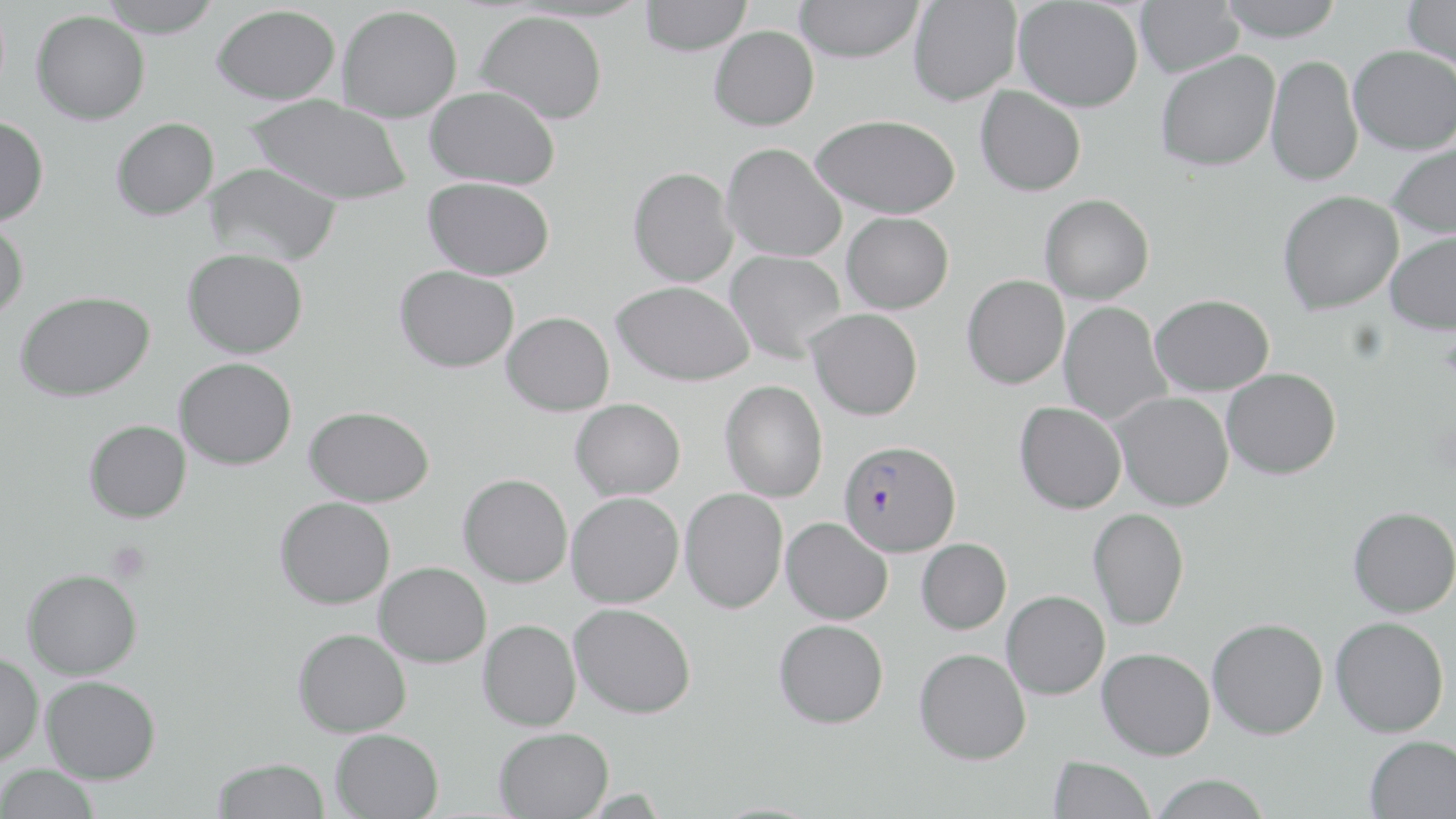
Approximate bounding boxes as [x1, y1, x2, y2] in pixels. Uninfected red blood cell locations: [97, 0, 223, 37], [640, 0, 751, 55], [1215, 0, 1344, 41], [1403, 0, 1456, 72], [794, 1, 924, 63], [908, 1, 1021, 106], [1014, 1, 1143, 112], [1135, 1, 1242, 77], [212, 4, 340, 105], [337, 5, 462, 123], [31, 10, 150, 125], [475, 10, 607, 124], [709, 25, 819, 130], [1348, 45, 1456, 155], [1155, 51, 1279, 172], [1265, 54, 1363, 187], [425, 85, 560, 189], [975, 86, 1086, 196], [247, 95, 412, 206], [810, 114, 961, 219], [0, 116, 49, 226], [111, 117, 219, 220], [1386, 140, 1456, 238], [722, 142, 847, 262], [203, 162, 342, 265], [628, 167, 738, 287], [422, 177, 554, 280], [1277, 190, 1403, 314], [1040, 194, 1154, 304], [842, 211, 954, 314], [0, 218, 29, 318], [1384, 232, 1456, 335], [182, 248, 308, 359], [725, 250, 846, 362], [394, 265, 519, 373], [961, 275, 1069, 389], [612, 280, 755, 386], [15, 291, 155, 402], [1149, 294, 1274, 396], [1058, 301, 1171, 425], [807, 309, 922, 420], [502, 311, 614, 415], [173, 357, 297, 470], [1221, 367, 1341, 479], [720, 380, 828, 501], [1110, 392, 1234, 511], [570, 398, 685, 500], [1014, 402, 1126, 514], [304, 406, 436, 506], [84, 419, 191, 523], [458, 473, 573, 587], [679, 487, 789, 613], [566, 492, 684, 607], [275, 497, 395, 609], [1347, 506, 1456, 618], [1088, 508, 1189, 630], [781, 517, 893, 624], [916, 539, 1011, 634], [374, 561, 491, 667], [22, 568, 142, 679], [1001, 590, 1110, 699], [569, 603, 696, 718], [1330, 616, 1449, 737], [1207, 618, 1328, 739], [478, 619, 581, 731], [774, 619, 888, 728], [293, 628, 412, 737], [914, 647, 1031, 764], [1096, 647, 1215, 760], [0, 652, 44, 766], [41, 675, 161, 784], [494, 727, 613, 819], [330, 728, 444, 819], [1365, 734, 1456, 817], [1048, 756, 1156, 818], [212, 757, 329, 818], [1, 763, 99, 819], [1148, 773, 1272, 818]. Plasmodium falciparum-infected red blood cell locations: [838, 439, 961, 556]. Platelet locations: [105, 541, 152, 583]. Slide-level diagnosis: Plasmodium falciparum. May-Grünwald-Giemsa-stained preparation. Thin blood smear. Image is 1456×819 pixels. Captured at 1000x magnification. Optical microscopy. Single field of view.